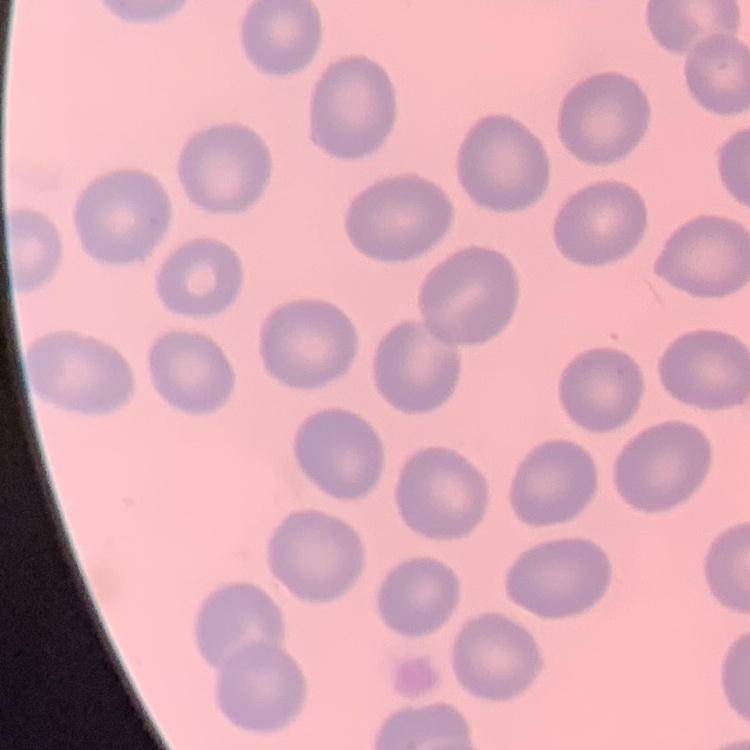

red blood cell morphology = no rouleaux formation
stain = Field's or Giemsa
image type = one tile cut from a larger photomicrograph
preparation = thin peripheral smear